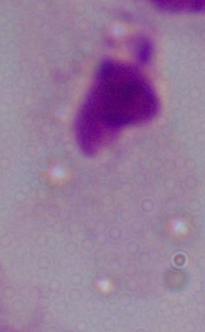
identification = trichomonad
magnification = 1000x
modality = photomicrograph